Outline each uninfected red blood cell.
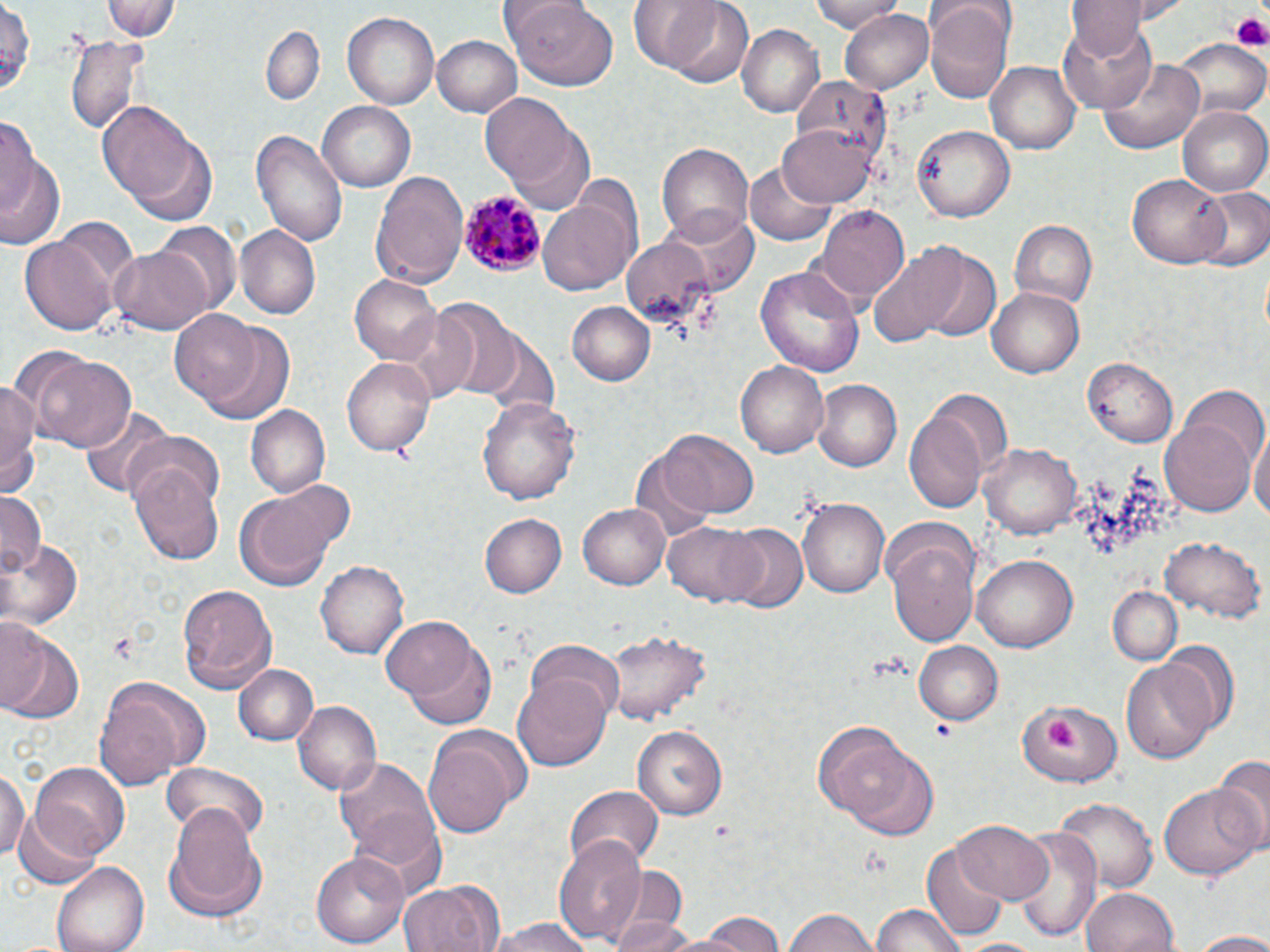

Approximate bounding boxes as named x1/y1/x2/y2 corners in pixels.
Uninfected red blood cells: (x1=105, y1=0, x2=179, y2=42), (x1=503, y1=0, x2=622, y2=88), (x1=652, y1=0, x2=755, y2=87), (x1=809, y1=0, x2=906, y2=33), (x1=1065, y1=0, x2=1152, y2=55), (x1=926, y1=5, x2=1012, y2=105), (x1=839, y1=8, x2=934, y2=93), (x1=343, y1=11, x2=439, y2=112), (x1=1058, y1=18, x2=1157, y2=113), (x1=260, y1=25, x2=325, y2=104), (x1=739, y1=26, x2=824, y2=119), (x1=65, y1=34, x2=147, y2=136), (x1=432, y1=34, x2=525, y2=116), (x1=1172, y1=38, x2=1269, y2=119), (x1=1101, y1=58, x2=1206, y2=153), (x1=988, y1=63, x2=1080, y2=154), (x1=482, y1=91, x2=585, y2=194), (x1=318, y1=101, x2=416, y2=193), (x1=99, y1=103, x2=202, y2=206), (x1=1181, y1=103, x2=1270, y2=196), (x1=0, y1=115, x2=41, y2=209), (x1=777, y1=121, x2=878, y2=209), (x1=912, y1=124, x2=1013, y2=223), (x1=250, y1=130, x2=346, y2=247), (x1=128, y1=135, x2=218, y2=226), (x1=656, y1=141, x2=755, y2=247), (x1=0, y1=153, x2=64, y2=252), (x1=745, y1=156, x2=840, y2=245), (x1=372, y1=167, x2=468, y2=292), (x1=1128, y1=173, x2=1230, y2=268), (x1=1192, y1=187, x2=1270, y2=275), (x1=536, y1=194, x2=636, y2=296), (x1=815, y1=204, x2=910, y2=304), (x1=669, y1=207, x2=757, y2=292), (x1=1010, y1=220, x2=1097, y2=310), (x1=154, y1=221, x2=242, y2=312), (x1=233, y1=226, x2=321, y2=321), (x1=22, y1=233, x2=120, y2=336), (x1=621, y1=238, x2=715, y2=325), (x1=866, y1=243, x2=967, y2=347), (x1=109, y1=244, x2=212, y2=333), (x1=913, y1=248, x2=1003, y2=344), (x1=756, y1=265, x2=866, y2=378), (x1=350, y1=273, x2=443, y2=367), (x1=988, y1=285, x2=1085, y2=376), (x1=567, y1=300, x2=655, y2=385), (x1=395, y1=307, x2=481, y2=401), (x1=169, y1=310, x2=262, y2=407), (x1=197, y1=322, x2=297, y2=426), (x1=32, y1=354, x2=138, y2=454), (x1=342, y1=357, x2=434, y2=458), (x1=1085, y1=357, x2=1180, y2=446), (x1=738, y1=362, x2=828, y2=457), (x1=0, y1=378, x2=41, y2=490), (x1=814, y1=380, x2=902, y2=469), (x1=1155, y1=393, x2=1264, y2=518), (x1=478, y1=396, x2=582, y2=505), (x1=905, y1=403, x2=992, y2=514), (x1=247, y1=405, x2=332, y2=497), (x1=79, y1=406, x2=174, y2=498), (x1=1251, y1=422, x2=1269, y2=530), (x1=120, y1=427, x2=228, y2=513), (x1=656, y1=429, x2=760, y2=519), (x1=980, y1=445, x2=1081, y2=538), (x1=128, y1=463, x2=225, y2=566), (x1=267, y1=478, x2=356, y2=559), (x1=234, y1=486, x2=341, y2=590), (x1=0, y1=492, x2=43, y2=580), (x1=801, y1=497, x2=890, y2=597), (x1=578, y1=504, x2=671, y2=590), (x1=479, y1=513, x2=566, y2=598), (x1=662, y1=521, x2=766, y2=607), (x1=723, y1=523, x2=810, y2=615), (x1=1161, y1=536, x2=1264, y2=624), (x1=1, y1=537, x2=81, y2=630), (x1=887, y1=537, x2=981, y2=649), (x1=972, y1=553, x2=1078, y2=652), (x1=317, y1=558, x2=409, y2=660), (x1=176, y1=582, x2=277, y2=693), (x1=1109, y1=586, x2=1182, y2=666), (x1=382, y1=616, x2=483, y2=706), (x1=0, y1=626, x2=83, y2=725), (x1=603, y1=628, x2=710, y2=729), (x1=402, y1=638, x2=498, y2=731), (x1=528, y1=640, x2=627, y2=722), (x1=914, y1=640, x2=1002, y2=725), (x1=1159, y1=641, x2=1238, y2=742), (x1=1121, y1=657, x2=1217, y2=764), (x1=235, y1=664, x2=319, y2=747), (x1=514, y1=673, x2=611, y2=771), (x1=96, y1=683, x2=191, y2=788), (x1=1015, y1=697, x2=1124, y2=785), (x1=292, y1=701, x2=380, y2=794), (x1=632, y1=725, x2=728, y2=821), (x1=824, y1=731, x2=938, y2=838), (x1=423, y1=738, x2=519, y2=841), (x1=335, y1=755, x2=440, y2=856), (x1=1213, y1=757, x2=1270, y2=848), (x1=0, y1=763, x2=30, y2=867), (x1=26, y1=764, x2=128, y2=868), (x1=159, y1=765, x2=266, y2=848), (x1=1160, y1=782, x2=1265, y2=877), (x1=566, y1=784, x2=663, y2=869), (x1=1052, y1=793, x2=1156, y2=892), (x1=165, y1=801, x2=265, y2=911), (x1=12, y1=809, x2=106, y2=889), (x1=349, y1=812, x2=447, y2=900), (x1=951, y1=818, x2=1055, y2=906), (x1=1011, y1=826, x2=1103, y2=945), (x1=552, y1=836, x2=648, y2=945), (x1=922, y1=842, x2=1012, y2=943), (x1=311, y1=850, x2=410, y2=949), (x1=53, y1=862, x2=149, y2=952), (x1=599, y1=865, x2=689, y2=952), (x1=398, y1=879, x2=500, y2=952), (x1=1082, y1=886, x2=1179, y2=952), (x1=869, y1=904, x2=967, y2=952), (x1=781, y1=906, x2=881, y2=952), (x1=692, y1=912, x2=792, y2=952), (x1=605, y1=915, x2=701, y2=952), (x1=484, y1=918, x2=598, y2=952), (x1=1186, y1=931, x2=1270, y2=951), (x1=956, y1=937, x2=1046, y2=952).

Summary:
  - Platelet locations: (x1=1228, y1=10, x2=1269, y2=49), (x1=1041, y1=720, x2=1086, y2=751), (x1=931, y1=721, x2=951, y2=738), (x1=711, y1=822, x2=735, y2=838)
  - Plasmodium malariae-infected red blood cell locations: (x1=458, y1=188, x2=547, y2=277)
  - Slide-level diagnosis: Plasmodium malariae
  - Field of view: one of a larger specimen
  - Magnification: 1000x
  - Image size: 1270×952 pixels
  - Stain: May-Grünwald-Giemsa
  - Modality: light microscopy
  - Preparation: thin blood film